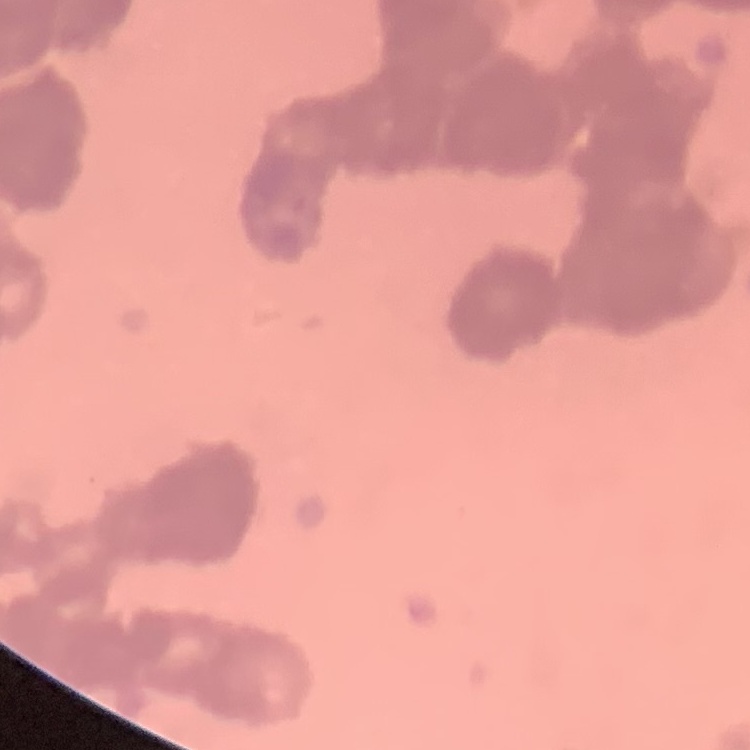

Summary:
  - Erythrocyte morphology: rouleaux formation
  - Image type: one tile cut from a larger photomicrograph
  - Preparation: thin blood smear
  - Stain: Field's or Giemsa